Report the malaria status of this cell.
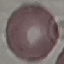

It is uninfected.

image_type: cell patch, automatically extracted from a larger field of view and resized to 64 × 64 pixels
preparation: thin blood smear
capture: smartphone through the microscope eyepiece
stain: Giemsa